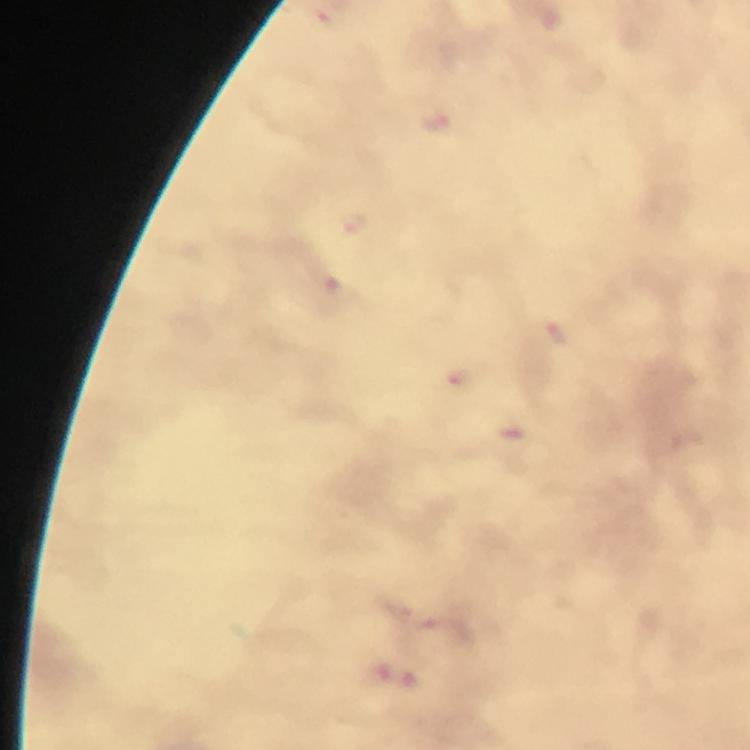

Approximate object centers, in pixels from the top-left corner.
Summary:
  - Plasmodium parasite locations: (x=438, y=125), (x=355, y=227), (x=558, y=335), (x=464, y=382), (x=517, y=434)
  - Preparation: thick blood smear
  - Immersion oil: applied
  - Stain: Giemsa
  - Magnification: 100x
  - Cropped from: a single field of view
  - Image size: 750×750 pixels
  - Capture: smartphone mounted on the microscope
  - Context: from a malaria diagnostic workup